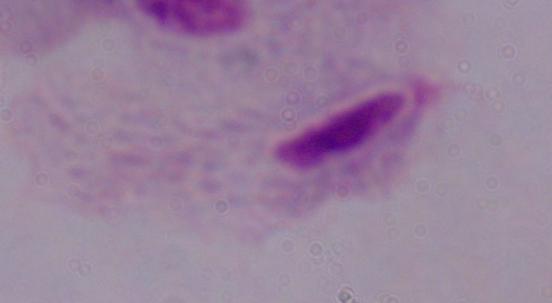
{
  "modality": "micrograph",
  "identification": "trichomonad",
  "magnification": "1000x"
}